Report the malaria status of this cell.
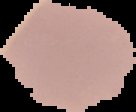

Uninfected.

{
  "image_type": "cell region segmented out of the field of view; surrounding area masked to black",
  "image_size": "136×112 pixels",
  "preparation": "thin blood smear"
}